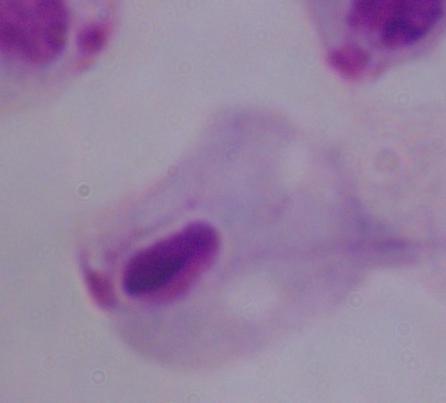
Micrograph. A trichomonad is seen. Captured at 1000x magnification.